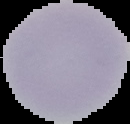

preparation = thin blood smear
image size = 130×124 pixels
result = no malaria parasites detected
image type = cell region segmented out of the field of view; surrounding area masked to black